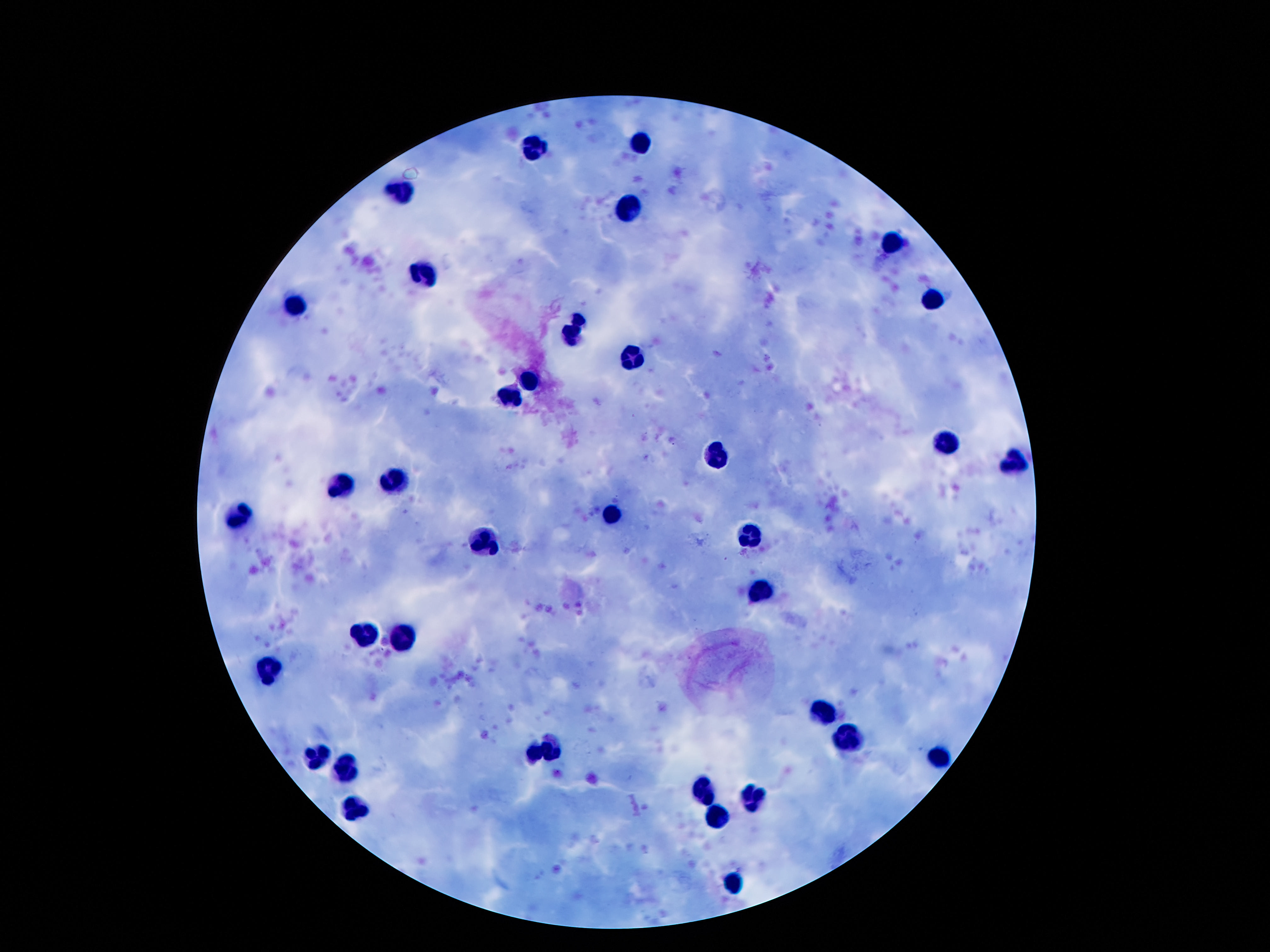 Approximate object centers, in pixels from the top-left corner. Leukocyte locations: (x=641, y=144), (x=535, y=148), (x=399, y=195), (x=628, y=210), (x=891, y=244), (x=423, y=273), (x=934, y=297), (x=292, y=303), (x=576, y=329), (x=632, y=355), (x=533, y=376), (x=509, y=395), (x=945, y=441), (x=723, y=456), (x=1018, y=460), (x=395, y=479), (x=339, y=486), (x=611, y=514), (x=240, y=518), (x=749, y=538), (x=486, y=544), (x=365, y=633), (x=400, y=638), (x=276, y=667), (x=824, y=712), (x=846, y=738), (x=555, y=751), (x=534, y=752), (x=316, y=755), (x=936, y=755), (x=345, y=764), (x=703, y=792), (x=759, y=796), (x=355, y=808), (x=718, y=816), (x=736, y=882). Giemsa-stained preparation. Image is 1270×952 pixels. Thick blood smear. One field from this slide. 100x magnification. Patient malaria status: negative. Photographed through the microscope eyepiece with a smartphone camera.